Comment on the morphology of the erythrocytes.
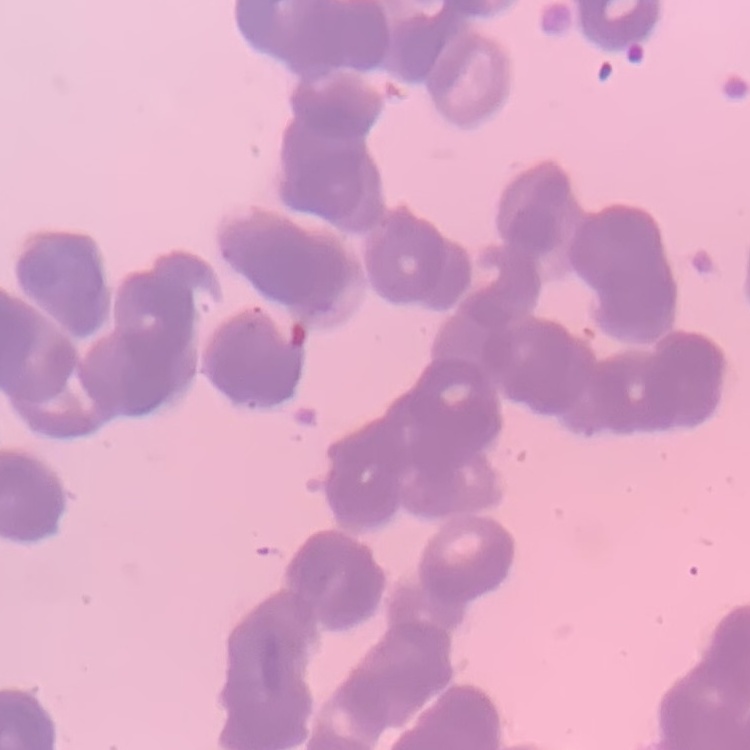

They show rouleaux formation.

Square crop of a larger photomicrograph. Thin blood film. Stained with either Field's or Giemsa.